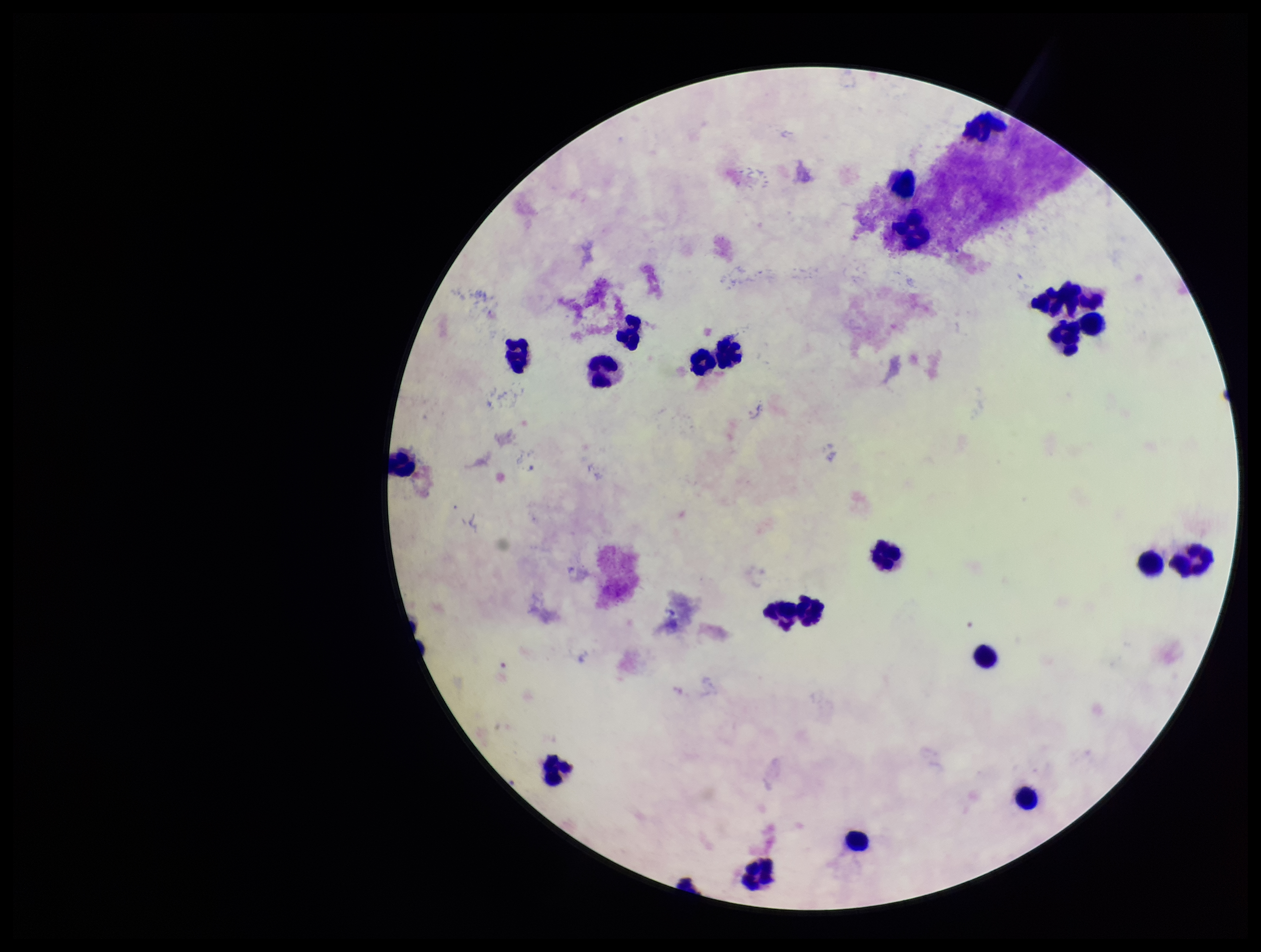
capture = smartphone photograph through the microscope eyepiece
preparation = thick smear
leukocyte count = 23
stain = Giemsa
Plasmodium parasites = none identified
field of view = single
image size = 1261×952 pixels
patient malaria status = negative
parasite count = 0